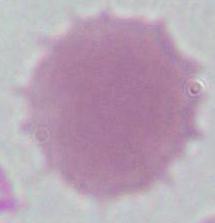

magnification = 1000x
identification = red blood cell
modality = micrograph